Comment on the morphology of the red blood cells.
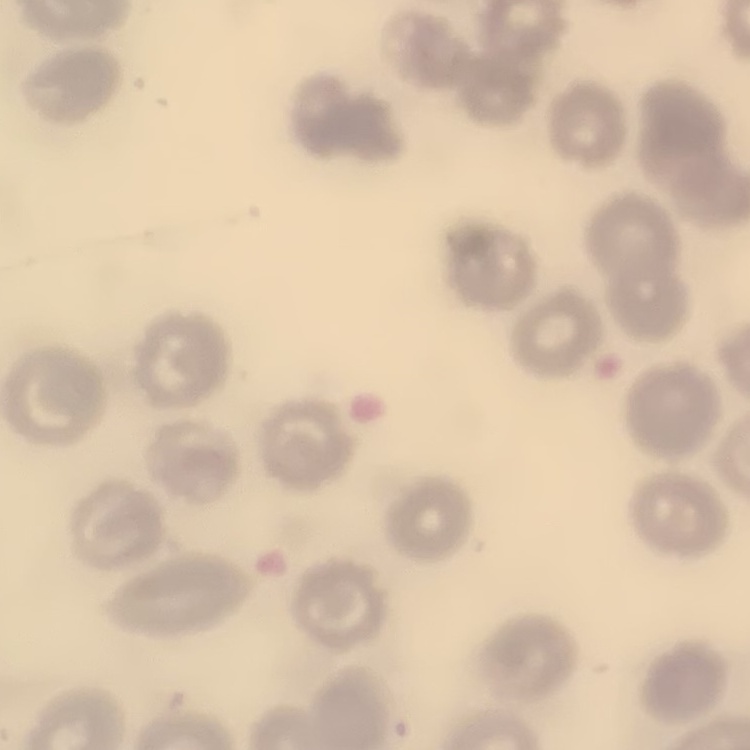
No rouleaux formation.

Summary:
  - Stain: Field's or Giemsa
  - Preparation: thin peripheral smear
  - Image type: square crop of a larger photomicrograph